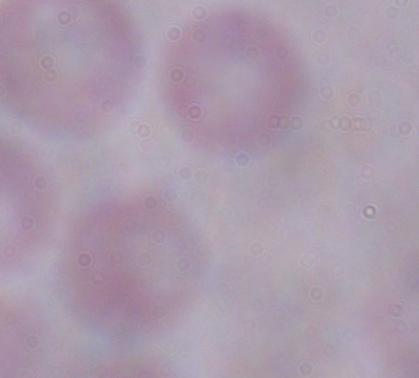 Micrograph. Captured at 1000x magnification. A trypanosome is shown.